Classify this cell by malaria status.
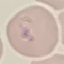

It is parasitized.

capture = smartphone through the microscope eyepiece
preparation = thin blood film
image type = cell patch, automatically extracted from a larger field of view and resized to 64 × 64 pixels
stain = Giemsa